Comment on the morphology of the erythrocytes.
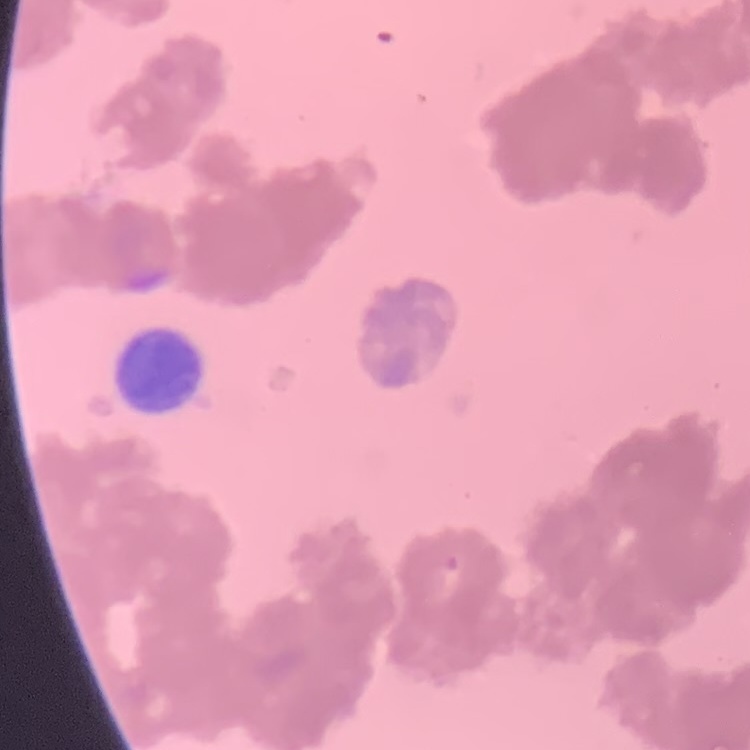
They show rouleaux formation.

One tile cut from a larger photomicrograph. Stained with either Field's or Giemsa. Thin peripheral smear.